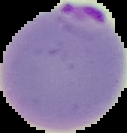

Summary:
  - Preparation: thin blood film
  - Malaria status: parasitized
  - Image size: 127×133 pixels
  - Image type: cell region segmented out of the field of view; surrounding area masked to black